Assess this cell for malaria.
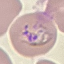

Parasitized.

Summary:
  - Stain: Giemsa
  - Capture: smartphone camera at the microscope eyepiece
  - Image type: automatically extracted cell patch, resized to 64 × 64 pixels
  - Preparation: thin blood smear